Comment on the morphology of the erythrocytes.
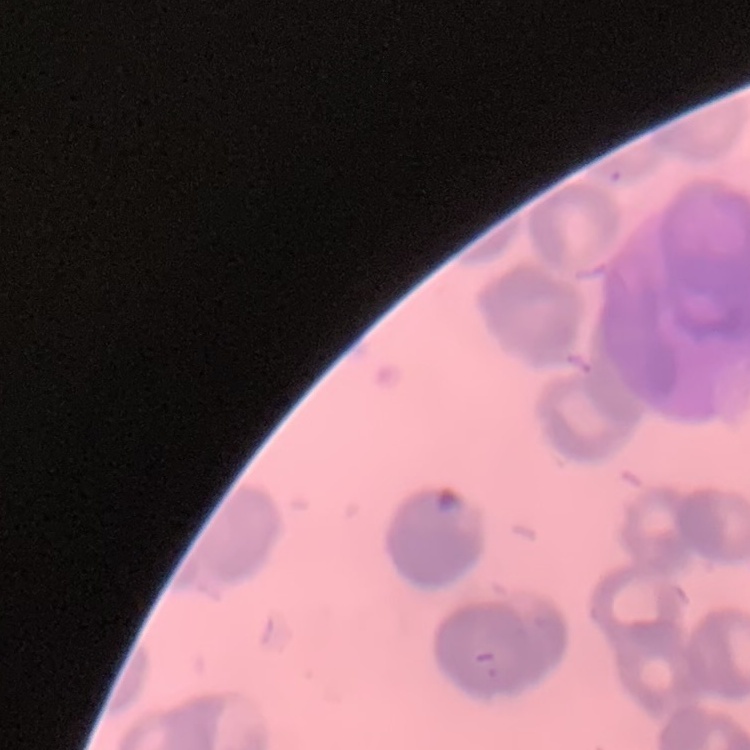
Rouleaux formation.

{
  "stain": "Field's or Giemsa",
  "image_type": "square crop of a larger photomicrograph",
  "preparation": "thin peripheral smear"
}